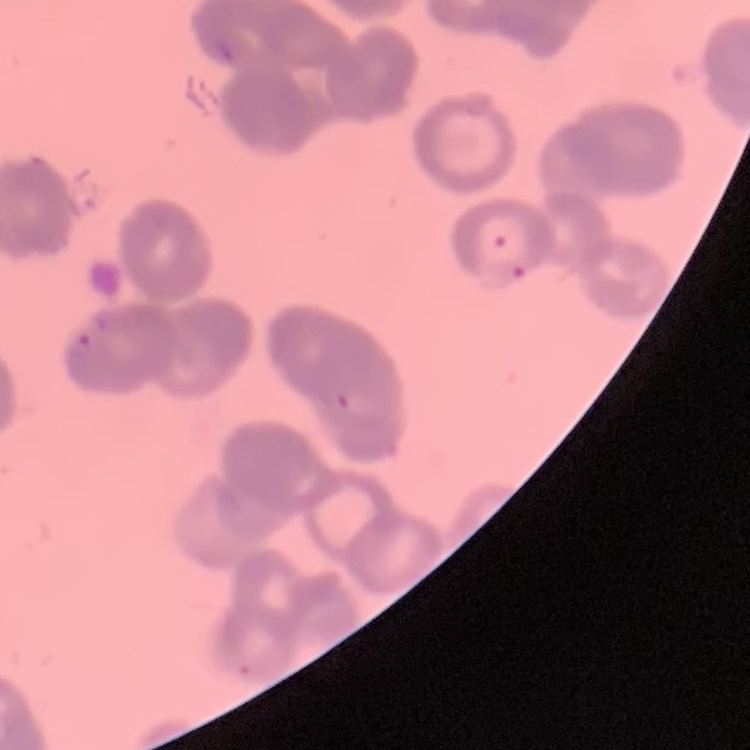

The erythrocytes show rouleaux formation. Thin blood smear. Stained with either Field's or Giemsa. Square crop of a larger photomicrograph.